Classify this cell by malaria status.
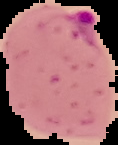
Parasitized.

From a thin blood smear. Cell region segmented out of the field of view; the surrounding area is masked to black. Image is 118×145 pixels.